Mark where platelets are.
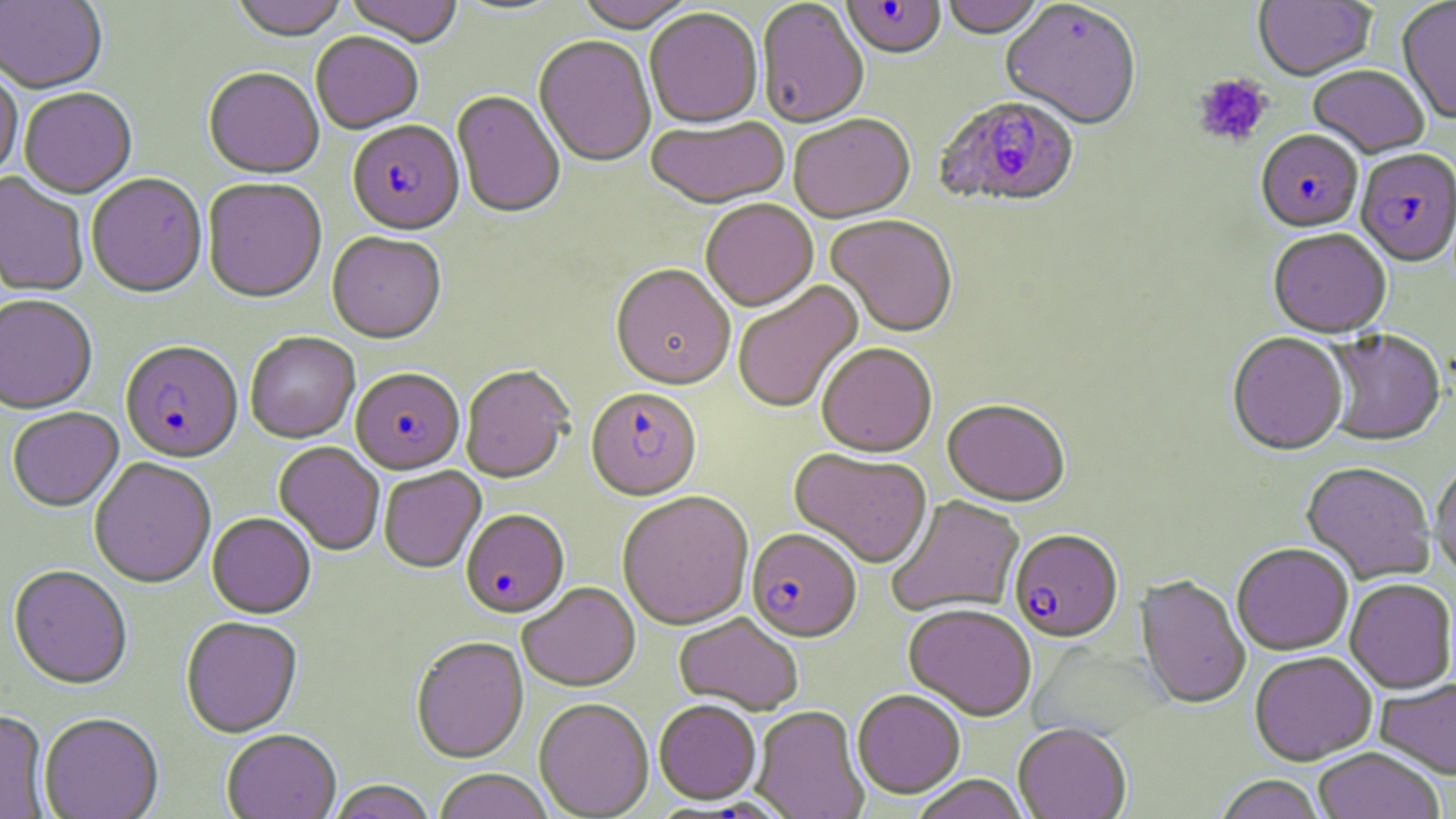
Approximate bounding boxes as named x1/y1/x2/y2 corners in pixels.
Platelets: (x1=1192, y1=74, x2=1273, y2=149).

Plasmodium falciparum-infected red blood cell locations: (x1=841, y1=1, x2=946, y2=61), (x1=934, y1=97, x2=1080, y2=211), (x1=348, y1=123, x2=464, y2=238), (x1=1256, y1=132, x2=1363, y2=235), (x1=1355, y1=151, x2=1456, y2=269), (x1=120, y1=344, x2=243, y2=465), (x1=351, y1=370, x2=465, y2=476), (x1=586, y1=389, x2=702, y2=503), (x1=461, y1=511, x2=570, y2=620), (x1=746, y1=530, x2=861, y2=644), (x1=1010, y1=531, x2=1123, y2=644). Uninfected red blood cell locations: (x1=0, y1=0, x2=107, y2=95), (x1=230, y1=0, x2=348, y2=43), (x1=344, y1=0, x2=464, y2=49), (x1=574, y1=0, x2=698, y2=35), (x1=941, y1=0, x2=1048, y2=41), (x1=756, y1=1, x2=869, y2=131), (x1=1254, y1=1, x2=1377, y2=83), (x1=1397, y1=1, x2=1456, y2=125), (x1=1001, y1=3, x2=1141, y2=132), (x1=645, y1=10, x2=763, y2=132), (x1=311, y1=33, x2=423, y2=136), (x1=534, y1=37, x2=656, y2=169), (x1=0, y1=65, x2=23, y2=185), (x1=1308, y1=67, x2=1429, y2=160), (x1=203, y1=71, x2=324, y2=181), (x1=20, y1=90, x2=137, y2=201), (x1=451, y1=93, x2=565, y2=220), (x1=789, y1=116, x2=916, y2=225), (x1=646, y1=118, x2=791, y2=211), (x1=0, y1=173, x2=89, y2=298), (x1=87, y1=175, x2=207, y2=300), (x1=202, y1=179, x2=327, y2=305), (x1=701, y1=201, x2=819, y2=313), (x1=825, y1=216, x2=958, y2=339), (x1=1268, y1=231, x2=1391, y2=341), (x1=327, y1=234, x2=446, y2=346), (x1=610, y1=266, x2=736, y2=393), (x1=732, y1=281, x2=865, y2=414), (x1=0, y1=297, x2=98, y2=416), (x1=1324, y1=330, x2=1445, y2=448), (x1=245, y1=334, x2=360, y2=445), (x1=1227, y1=334, x2=1348, y2=457), (x1=817, y1=345, x2=937, y2=460), (x1=460, y1=367, x2=574, y2=485), (x1=942, y1=401, x2=1070, y2=508), (x1=7, y1=409, x2=124, y2=514), (x1=274, y1=442, x2=385, y2=556), (x1=789, y1=451, x2=932, y2=570), (x1=89, y1=459, x2=217, y2=590), (x1=1431, y1=459, x2=1456, y2=580), (x1=1300, y1=463, x2=1436, y2=586), (x1=379, y1=468, x2=486, y2=575), (x1=616, y1=493, x2=755, y2=632), (x1=886, y1=496, x2=1025, y2=619), (x1=207, y1=514, x2=316, y2=620), (x1=1232, y1=544, x2=1353, y2=657), (x1=8, y1=567, x2=132, y2=692), (x1=1135, y1=576, x2=1250, y2=711), (x1=1344, y1=580, x2=1456, y2=695), (x1=518, y1=584, x2=641, y2=693), (x1=903, y1=605, x2=1036, y2=722), (x1=673, y1=614, x2=803, y2=716), (x1=181, y1=618, x2=303, y2=739), (x1=410, y1=638, x2=529, y2=764), (x1=1249, y1=652, x2=1377, y2=766), (x1=1375, y1=679, x2=1456, y2=780), (x1=852, y1=690, x2=965, y2=799), (x1=534, y1=700, x2=654, y2=818), (x1=654, y1=702, x2=761, y2=806), (x1=751, y1=707, x2=869, y2=819), (x1=0, y1=711, x2=50, y2=818), (x1=38, y1=715, x2=164, y2=819), (x1=1013, y1=724, x2=1131, y2=819), (x1=222, y1=731, x2=341, y2=819), (x1=1313, y1=748, x2=1445, y2=819), (x1=433, y1=770, x2=554, y2=819), (x1=1214, y1=775, x2=1327, y2=819), (x1=910, y1=776, x2=1030, y2=819), (x1=327, y1=781, x2=437, y2=819). Slide-level diagnosis: Plasmodium falciparum. May-Grünwald-Giemsa stain. Image is 1456×819 pixels. One field of a larger specimen. Optical microscopy. 1000x magnification. Thin blood film.